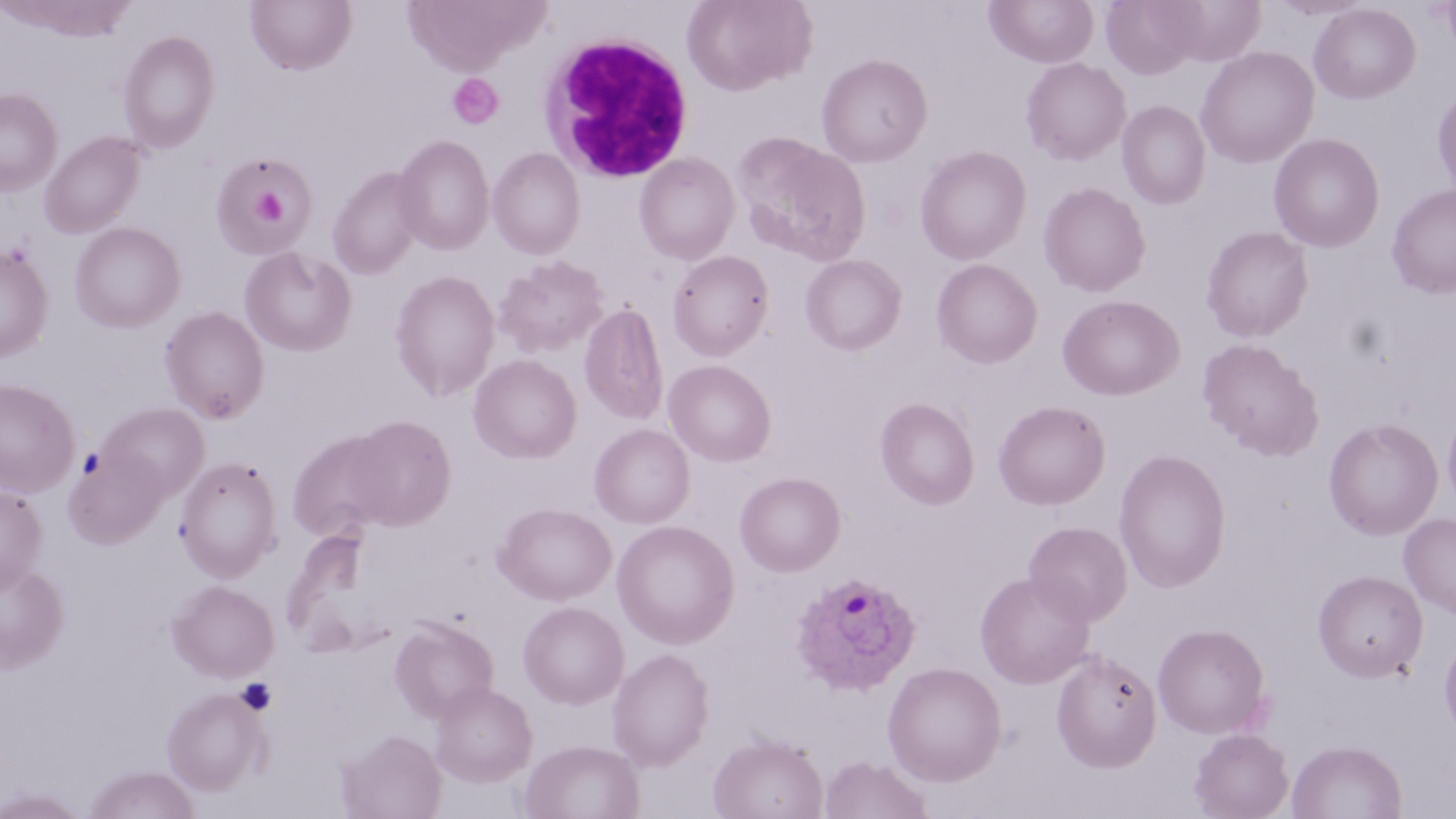 Approximate bounding boxes as named x1/y1/x2/y2 corners in pixels. Uninfected red blood cell locations: (x1=245, y1=0, x2=357, y2=75), (x1=400, y1=0, x2=548, y2=75), (x1=682, y1=0, x2=816, y2=95), (x1=1101, y1=0, x2=1205, y2=79), (x1=6, y1=1, x2=134, y2=39), (x1=985, y1=1, x2=1098, y2=68), (x1=1308, y1=3, x2=1420, y2=104), (x1=118, y1=30, x2=219, y2=153), (x1=1195, y1=47, x2=1319, y2=168), (x1=816, y1=53, x2=933, y2=167), (x1=1021, y1=57, x2=1131, y2=165), (x1=1432, y1=84, x2=1456, y2=199), (x1=0, y1=88, x2=62, y2=195), (x1=1117, y1=100, x2=1211, y2=209), (x1=39, y1=131, x2=144, y2=237), (x1=732, y1=131, x2=870, y2=266), (x1=1268, y1=132, x2=1385, y2=252), (x1=393, y1=135, x2=494, y2=253), (x1=915, y1=145, x2=1032, y2=265), (x1=487, y1=147, x2=585, y2=258), (x1=634, y1=153, x2=740, y2=264), (x1=212, y1=154, x2=316, y2=258), (x1=327, y1=167, x2=426, y2=279), (x1=1038, y1=181, x2=1151, y2=297), (x1=1386, y1=184, x2=1456, y2=298), (x1=69, y1=221, x2=185, y2=333), (x1=1201, y1=226, x2=1313, y2=342), (x1=0, y1=244, x2=53, y2=362), (x1=239, y1=247, x2=356, y2=356), (x1=667, y1=250, x2=774, y2=360), (x1=800, y1=254, x2=907, y2=354), (x1=492, y1=255, x2=610, y2=358), (x1=931, y1=259, x2=1043, y2=368), (x1=389, y1=270, x2=500, y2=400), (x1=1058, y1=295, x2=1183, y2=400), (x1=579, y1=302, x2=669, y2=426), (x1=160, y1=306, x2=269, y2=423), (x1=1197, y1=338, x2=1324, y2=460), (x1=469, y1=354, x2=581, y2=463), (x1=664, y1=360, x2=776, y2=466), (x1=0, y1=378, x2=80, y2=498), (x1=875, y1=398, x2=979, y2=509), (x1=993, y1=400, x2=1110, y2=509), (x1=99, y1=402, x2=209, y2=500), (x1=1442, y1=402, x2=1456, y2=516), (x1=347, y1=415, x2=456, y2=530), (x1=1323, y1=417, x2=1443, y2=540), (x1=589, y1=423, x2=695, y2=528), (x1=286, y1=431, x2=396, y2=541), (x1=64, y1=448, x2=167, y2=547), (x1=1114, y1=449, x2=1231, y2=592), (x1=175, y1=456, x2=283, y2=580), (x1=735, y1=472, x2=845, y2=576), (x1=0, y1=484, x2=48, y2=594), (x1=494, y1=502, x2=615, y2=606), (x1=1398, y1=512, x2=1456, y2=618), (x1=611, y1=520, x2=739, y2=649), (x1=1024, y1=521, x2=1132, y2=625), (x1=0, y1=559, x2=68, y2=671), (x1=1313, y1=570, x2=1428, y2=682), (x1=975, y1=571, x2=1095, y2=688), (x1=169, y1=581, x2=279, y2=681), (x1=518, y1=601, x2=629, y2=708), (x1=389, y1=616, x2=499, y2=723), (x1=1153, y1=623, x2=1270, y2=738), (x1=1439, y1=635, x2=1456, y2=743), (x1=607, y1=647, x2=714, y2=770), (x1=1051, y1=649, x2=1161, y2=772), (x1=882, y1=661, x2=1007, y2=785), (x1=429, y1=681, x2=537, y2=786), (x1=161, y1=687, x2=268, y2=794), (x1=1190, y1=728, x2=1293, y2=819), (x1=336, y1=729, x2=447, y2=819), (x1=708, y1=733, x2=828, y2=819), (x1=520, y1=739, x2=645, y2=819), (x1=1287, y1=739, x2=1407, y2=818), (x1=819, y1=755, x2=932, y2=819), (x1=83, y1=765, x2=199, y2=818), (x1=0, y1=787, x2=89, y2=818). White blood cell locations: (x1=539, y1=30, x2=695, y2=182). Platelet locations: (x1=447, y1=73, x2=503, y2=129), (x1=238, y1=174, x2=296, y2=237), (x1=235, y1=678, x2=277, y2=716). Plasmodium ovale-infected red blood cell locations: (x1=791, y1=571, x2=921, y2=695). Slide-level diagnosis: Plasmodium ovale. May-Grünwald-Giemsa stain. Captured at 1000x magnification. Light microscopy. Image is 1456×819 pixels. Thin blood smear. One field of a larger specimen.